Comment on the morphology of the erythrocytes.
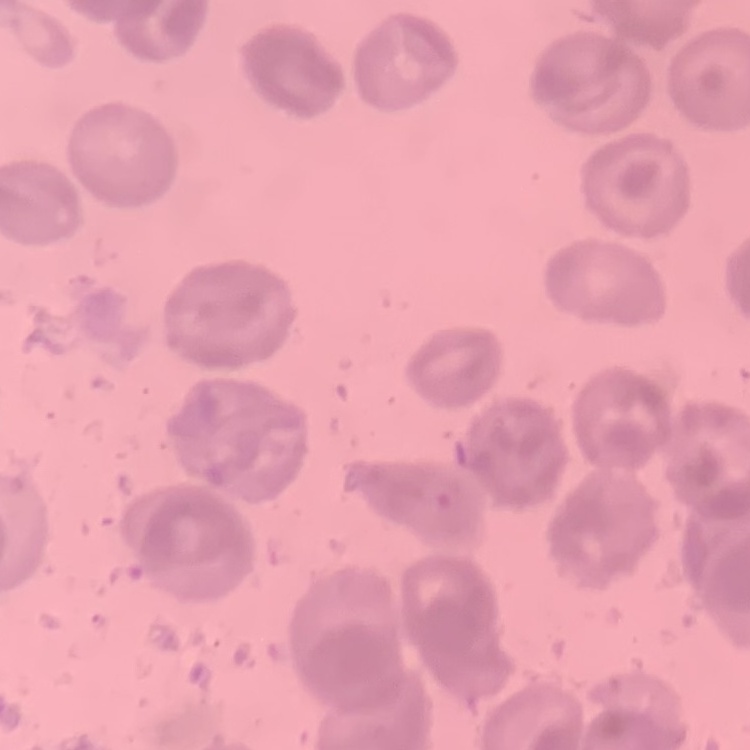
No rouleaux formation.

Summary:
  - Preparation: thin peripheral smear
  - Image type: one tile cut from a larger photomicrograph
  - Stain: Field's or Giemsa